Point out each leukocyte.
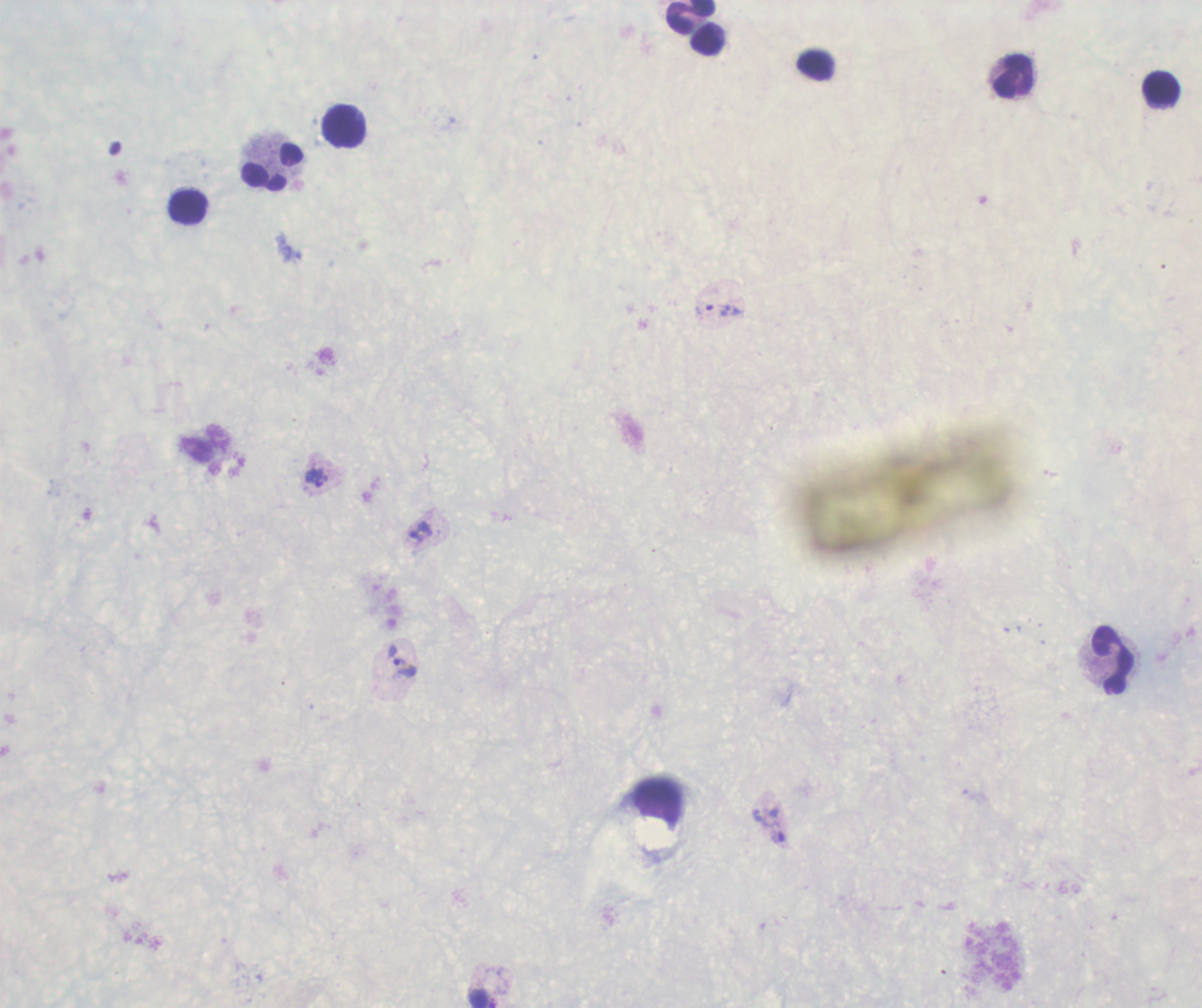

Approximate centers as (x, y) in pixels.
Leukocytes: (690, 17), (706, 39), (1014, 76), (1161, 90), (344, 126), (272, 166), (188, 206), (1112, 661).

Approximate centers as (x, y) in pixels.
Summary:
  - Trophozoite locations: (713, 310), (317, 477), (401, 661), (768, 827)
  - Image size: 1202×1008 pixels
  - Field of view: single
  - Result: Plasmodium parasites identified
  - Background quality: poor
  - Stain: Romanowsky
  - Coloration quality: bad
  - Preparation: thick smear of blood
  - Context: previously used in an actual diagnosis
  - Magnification: 100x